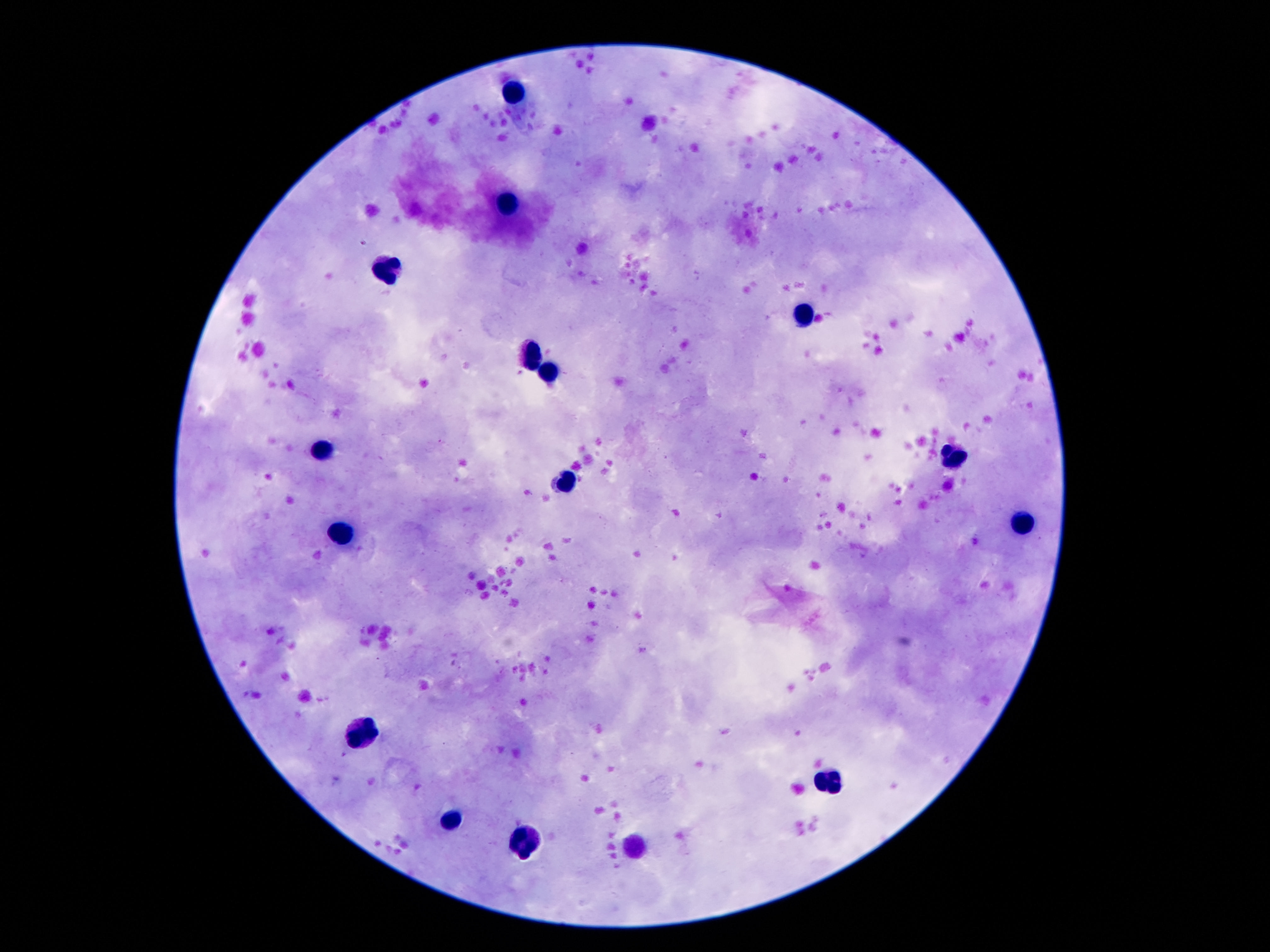
Approximate object centers, in pixels from the top-left corner.
Summary:
  - Leukocyte locations: (x=519, y=94), (x=509, y=204), (x=389, y=272), (x=805, y=314), (x=532, y=357), (x=548, y=375), (x=323, y=453), (x=955, y=458), (x=569, y=480), (x=1020, y=528), (x=344, y=539), (x=362, y=734), (x=832, y=784), (x=453, y=826), (x=525, y=843)
  - Stain: Giemsa
  - Patient malaria status: uninfected
  - Preparation: thick peripheral-blood smear
  - Field of view: one from this slide
  - Image size: 1270×952 pixels
  - Capture: smartphone camera through the microscope eyepiece
  - Magnification: 100x